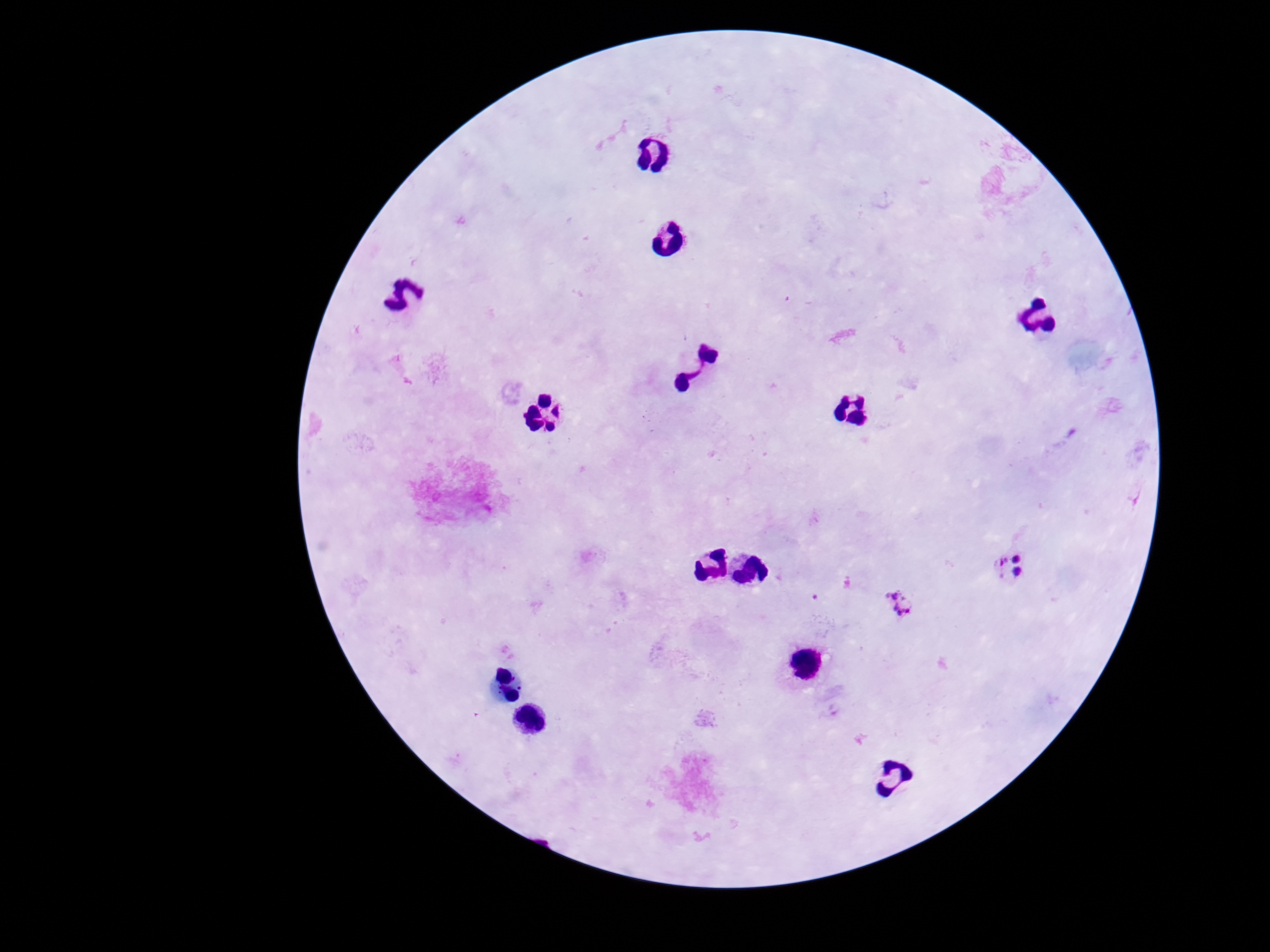
Approximate object centers, in pixels from the top-left corner.
Summary:
  - Plasmodium parasite locations: (x=1011, y=565), (x=899, y=606), (x=835, y=707)
  - Preparation: thick peripheral-blood smear
  - Capture: smartphone camera through the microscope eyepiece
  - Image size: 1270×952 pixels
  - Magnification: 100x
  - Stain: Giemsa
  - Patient malaria status: positive
  - Field of view: single